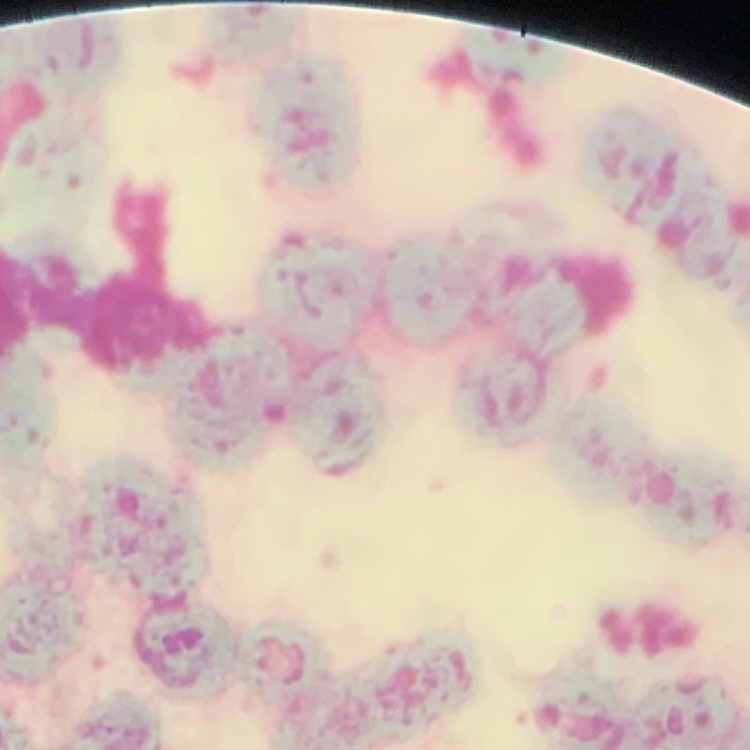 The red blood cells exhibit rouleaux formation. Stained with either Field's or Giemsa. Thin peripheral smear. One tile cut from a larger photomicrograph.